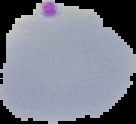

preparation = thin blood smear
image type = segmented cell region with the area outside set to black
image size = 136×124 pixels
result = malaria parasites detected